Identify the parasite.
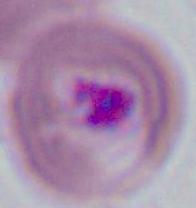

This is Plasmodium.

Summary:
  - Modality: micrograph
  - Magnification: 400x or 1000x